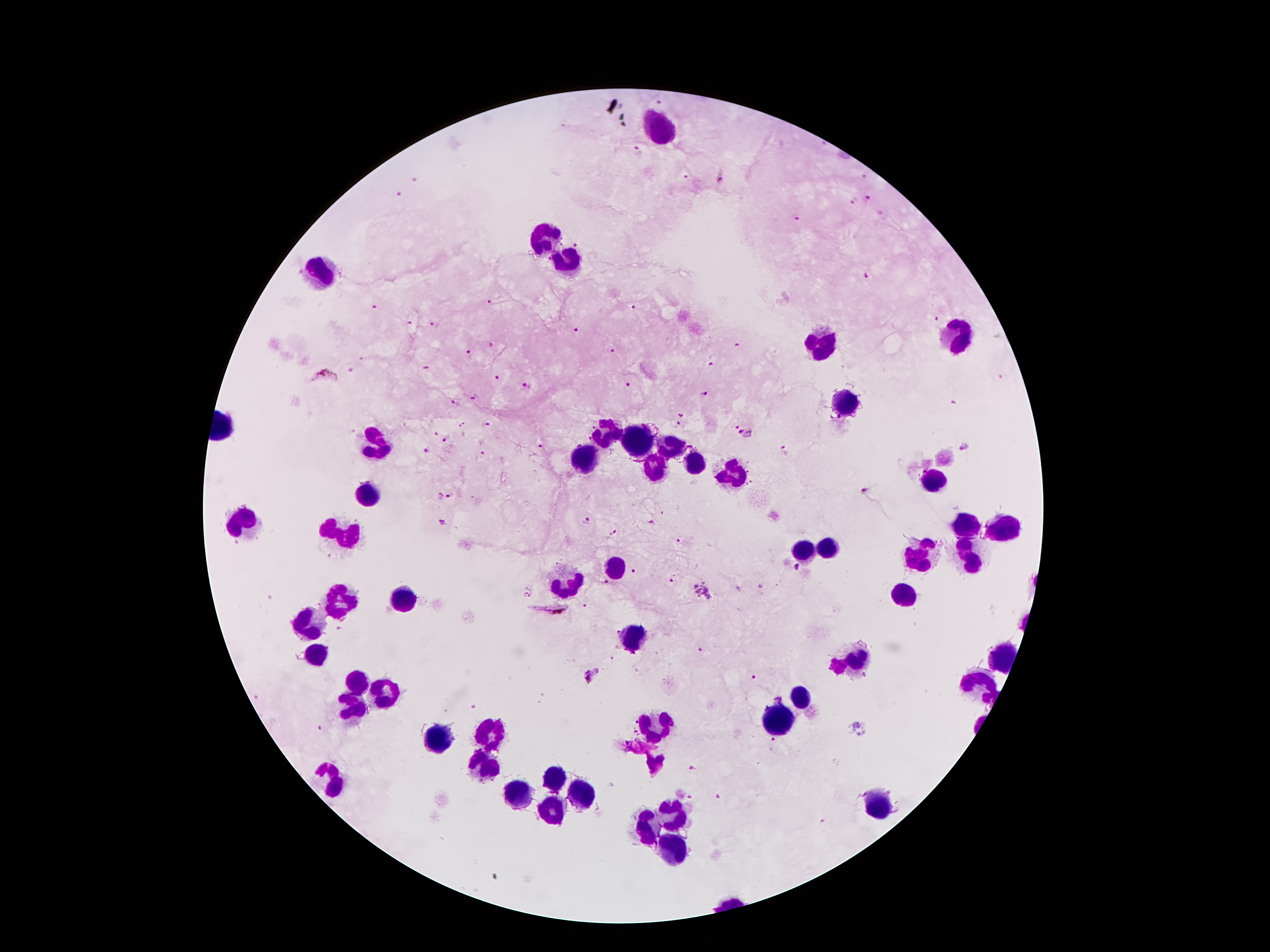
Approximate object centers, in pixels from the top-left corner.
Summary:
  - Leukocyte locations: (x=659, y=127), (x=545, y=238), (x=568, y=261), (x=323, y=276), (x=957, y=337), (x=820, y=343), (x=846, y=404), (x=604, y=433), (x=375, y=439), (x=636, y=441), (x=673, y=446), (x=583, y=454), (x=650, y=467), (x=696, y=467), (x=732, y=475), (x=936, y=479), (x=369, y=494), (x=247, y=523), (x=972, y=523), (x=1003, y=528), (x=344, y=534), (x=827, y=549), (x=799, y=551), (x=923, y=553), (x=969, y=557), (x=615, y=567), (x=566, y=582), (x=906, y=595), (x=337, y=599), (x=400, y=601), (x=308, y=626), (x=633, y=637), (x=316, y=653), (x=856, y=658), (x=1001, y=660), (x=360, y=683), (x=978, y=685), (x=386, y=693), (x=804, y=693), (x=352, y=712), (x=783, y=716), (x=657, y=725), (x=491, y=731), (x=442, y=742), (x=484, y=767), (x=327, y=775), (x=558, y=781), (x=579, y=794), (x=516, y=796), (x=877, y=807), (x=549, y=811), (x=671, y=815), (x=646, y=826), (x=669, y=851)
  - Malaria parasite locations: (x=658, y=102), (x=638, y=149), (x=685, y=175), (x=722, y=176), (x=865, y=178), (x=413, y=180), (x=398, y=194), (x=867, y=197), (x=853, y=201), (x=880, y=212), (x=796, y=218), (x=577, y=242), (x=864, y=276), (x=489, y=301), (x=374, y=307), (x=634, y=309), (x=934, y=316), (x=411, y=324), (x=432, y=324), (x=576, y=330), (x=489, y=344), (x=738, y=346), (x=611, y=351), (x=469, y=353), (x=711, y=366), (x=426, y=368), (x=351, y=369), (x=324, y=374), (x=496, y=378), (x=626, y=383), (x=526, y=385), (x=704, y=394), (x=475, y=396), (x=456, y=404), (x=681, y=415), (x=463, y=425), (x=485, y=425), (x=678, y=426), (x=433, y=431), (x=745, y=434), (x=446, y=438), (x=964, y=446), (x=539, y=448), (x=427, y=449), (x=784, y=451), (x=484, y=453), (x=863, y=491), (x=440, y=496), (x=449, y=497), (x=441, y=521), (x=588, y=521), (x=650, y=524), (x=613, y=533), (x=678, y=540), (x=797, y=567), (x=635, y=570), (x=671, y=581), (x=607, y=584), (x=527, y=594), (x=584, y=605), (x=551, y=612), (x=699, y=650), (x=594, y=676), (x=754, y=677), (x=319, y=729), (x=774, y=743), (x=692, y=769), (x=718, y=796)
  - Magnification: 100x
  - Field of view: one from this slide
  - Patient malaria status: infected with Plasmodium falciparum
  - Image size: 1270×952 pixels
  - Stain: Giemsa
  - Preparation: thick peripheral-blood smear
  - Capture: smartphone camera through the microscope eyepiece